Outline each blood parasite and name the species.
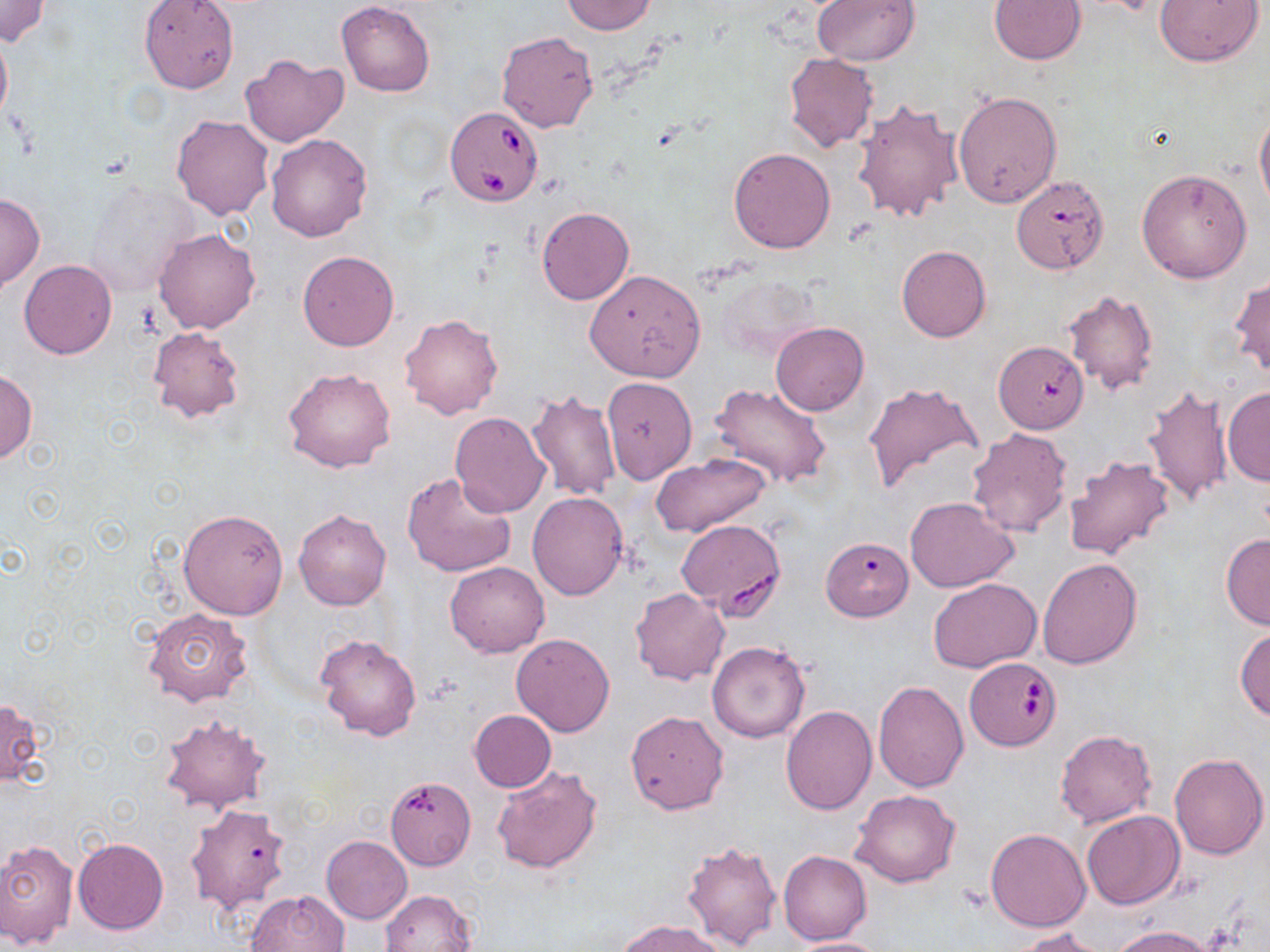
Approximate bounding boxes as named x1/y1/x2/y2 corners in pixels.
Babesia divergens-infected red blood cells: (x1=445, y1=105, x2=545, y2=208), (x1=676, y1=519, x2=786, y2=615), (x1=965, y1=658, x2=1061, y2=751).
No Plasmodium falciparum, Plasmodium ovale, Plasmodium malariae, Plasmodium vivax, or Trypanosoma brucei observed.

Uninfected red blood cell locations: (x1=559, y1=0, x2=656, y2=35), (x1=811, y1=0, x2=920, y2=67), (x1=988, y1=0, x2=1085, y2=65), (x1=1153, y1=0, x2=1264, y2=67), (x1=0, y1=1, x2=51, y2=46), (x1=138, y1=1, x2=240, y2=93), (x1=336, y1=2, x2=434, y2=97), (x1=0, y1=27, x2=12, y2=132), (x1=496, y1=30, x2=599, y2=133), (x1=784, y1=51, x2=879, y2=153), (x1=240, y1=52, x2=349, y2=148), (x1=953, y1=91, x2=1062, y2=207), (x1=851, y1=98, x2=964, y2=224), (x1=1255, y1=110, x2=1270, y2=213), (x1=171, y1=115, x2=273, y2=220), (x1=265, y1=133, x2=372, y2=241), (x1=728, y1=147, x2=836, y2=253), (x1=1136, y1=168, x2=1254, y2=284), (x1=1010, y1=177, x2=1109, y2=277), (x1=85, y1=179, x2=196, y2=296), (x1=0, y1=193, x2=43, y2=292), (x1=537, y1=207, x2=634, y2=304), (x1=153, y1=228, x2=263, y2=334), (x1=896, y1=244, x2=991, y2=342), (x1=298, y1=250, x2=398, y2=351), (x1=20, y1=260, x2=116, y2=360), (x1=584, y1=269, x2=707, y2=382), (x1=719, y1=275, x2=823, y2=362), (x1=1230, y1=276, x2=1270, y2=378), (x1=1063, y1=289, x2=1159, y2=395), (x1=400, y1=313, x2=503, y2=420), (x1=771, y1=322, x2=869, y2=416), (x1=146, y1=326, x2=246, y2=425), (x1=994, y1=340, x2=1089, y2=432), (x1=282, y1=367, x2=397, y2=473), (x1=0, y1=370, x2=37, y2=464), (x1=602, y1=377, x2=696, y2=484), (x1=861, y1=380, x2=983, y2=496), (x1=1142, y1=383, x2=1234, y2=507), (x1=708, y1=384, x2=831, y2=490), (x1=1223, y1=387, x2=1270, y2=487), (x1=527, y1=389, x2=622, y2=499), (x1=449, y1=412, x2=551, y2=517), (x1=967, y1=427, x2=1074, y2=539), (x1=649, y1=452, x2=771, y2=537), (x1=1063, y1=455, x2=1176, y2=561), (x1=402, y1=471, x2=518, y2=578), (x1=527, y1=491, x2=629, y2=601), (x1=905, y1=496, x2=1019, y2=592), (x1=177, y1=508, x2=288, y2=620), (x1=293, y1=508, x2=391, y2=611), (x1=1220, y1=533, x2=1270, y2=630), (x1=821, y1=536, x2=913, y2=621), (x1=1036, y1=556, x2=1143, y2=670), (x1=445, y1=561, x2=549, y2=657), (x1=929, y1=578, x2=1041, y2=673), (x1=630, y1=587, x2=729, y2=685), (x1=142, y1=608, x2=254, y2=707), (x1=1234, y1=627, x2=1270, y2=722), (x1=315, y1=633, x2=423, y2=742), (x1=512, y1=633, x2=616, y2=737), (x1=706, y1=642, x2=810, y2=743), (x1=874, y1=678, x2=967, y2=792), (x1=0, y1=698, x2=45, y2=786), (x1=780, y1=706, x2=877, y2=815), (x1=470, y1=710, x2=555, y2=792), (x1=625, y1=711, x2=728, y2=814), (x1=158, y1=713, x2=270, y2=815), (x1=1055, y1=729, x2=1156, y2=827), (x1=1169, y1=752, x2=1268, y2=859), (x1=491, y1=764, x2=603, y2=874), (x1=383, y1=775, x2=474, y2=876), (x1=851, y1=789, x2=961, y2=887), (x1=186, y1=803, x2=292, y2=914), (x1=1082, y1=811, x2=1185, y2=910), (x1=985, y1=827, x2=1090, y2=932), (x1=321, y1=836, x2=412, y2=924), (x1=73, y1=837, x2=168, y2=934), (x1=0, y1=839, x2=78, y2=947), (x1=682, y1=839, x2=783, y2=950), (x1=779, y1=851, x2=872, y2=945), (x1=245, y1=889, x2=350, y2=952), (x1=381, y1=889, x2=478, y2=952), (x1=617, y1=920, x2=727, y2=952), (x1=1110, y1=925, x2=1219, y2=952), (x1=1014, y1=927, x2=1108, y2=951), (x1=786, y1=936, x2=889, y2=952). Slide-level diagnosis: Babesia divergens. Optical microscopy. One field of a larger specimen. 1000x magnification. Thin blood film. Image is 1270×952 pixels. May-Grünwald-Giemsa stain.